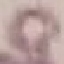
Summary:
  - Result: no malaria parasites seen
  - Image type: automatically extracted cell patch, resized to 64 × 64 pixels
  - Preparation: thin smear
  - Capture: smartphone camera at the microscope eyepiece
  - Stain: Giemsa